Report the malaria status.
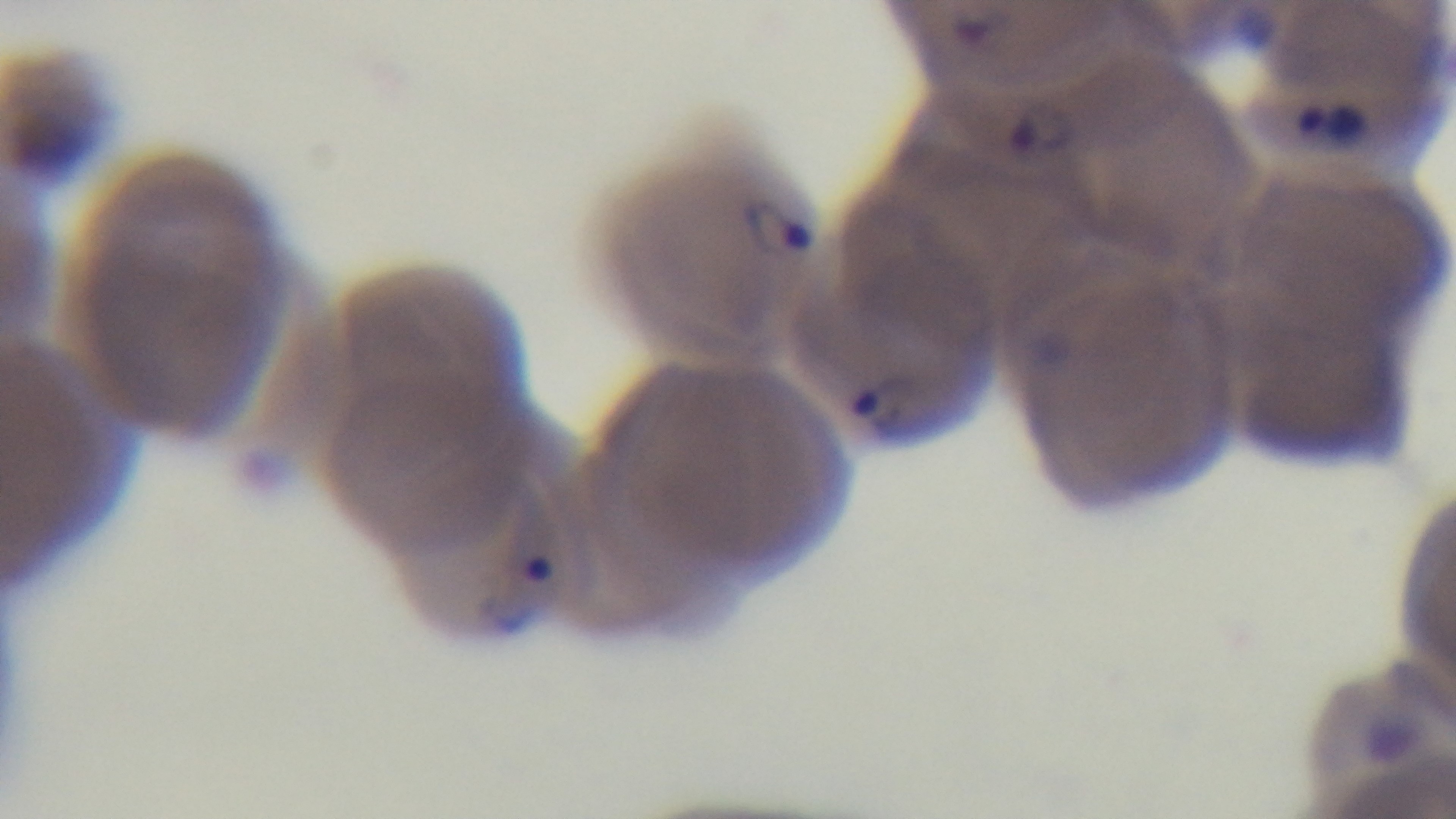
Positive.

capture = mounted 4K digital camera
stain = Giemsa
objective = 100x oil immersion
field of view = one from the slide
preparation = thin smear
modality = light microscopy